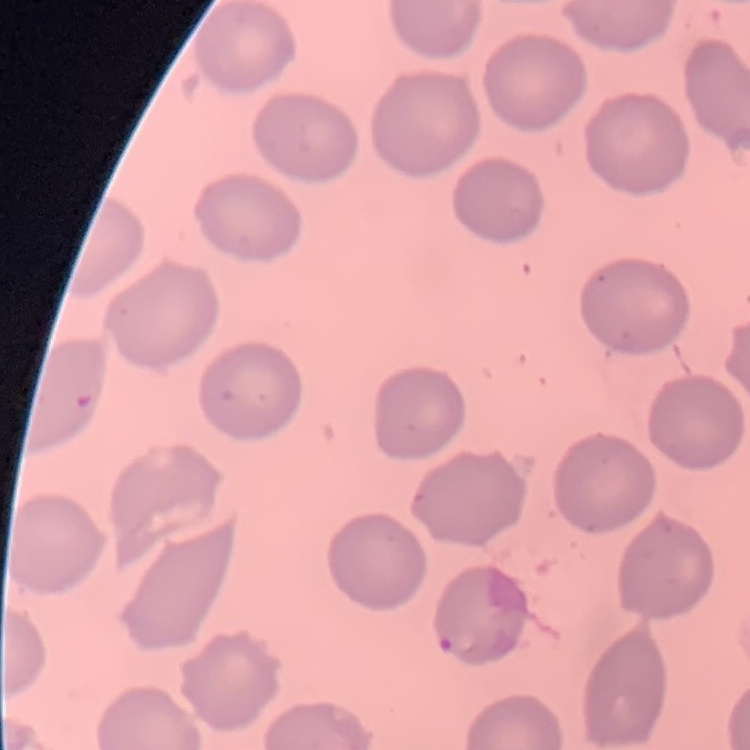
The erythrocytes show no rouleaux formation. Field's or Giemsa stain. Thin peripheral smear. One tile cut from a larger photomicrograph.